Report the malaria status of this cell.
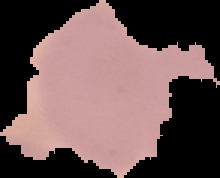

It is uninfected.

image_size: 220×178 pixels
preparation: thin blood film
image_type: cell region segmented out of the field of view; surrounding area masked to black